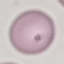

Malaria status: uninfected. Giemsa-stained preparation. Cell patch, automatically extracted from a larger field of view and resized to 64 × 64 pixels. Photographed with a smartphone camera at the microscope eyepiece. Thin smear of blood.